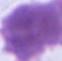

{
  "identification": "erythrocyte",
  "magnification": "1000x",
  "modality": "photomicrograph"
}